State which parasite is depicted.
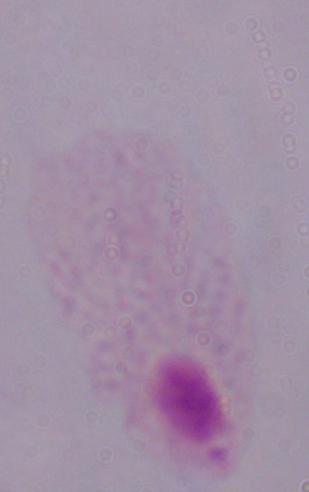

A trichomonad.

modality = photomicrograph
magnification = 1000x